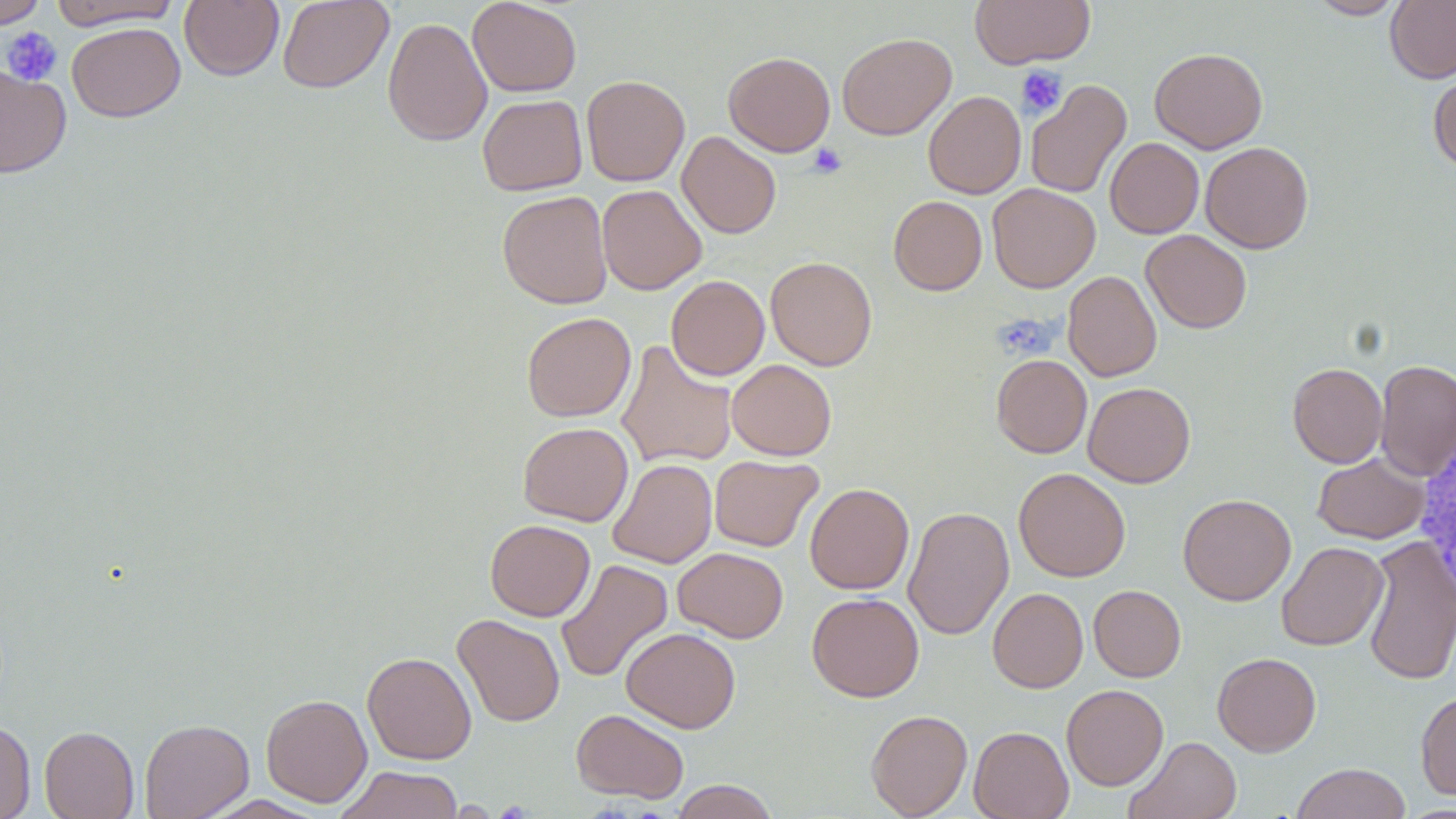

slide-level diagnosis = negative for blood parasites
magnification = 1000x
image size = 1456×819 pixels
uninfected red blood cell locations = approximate bounding boxes as [x1, y1, x2, y2] in pixels: [0, 0, 46, 29], [46, 0, 183, 30], [277, 0, 394, 93], [467, 0, 582, 97], [970, 0, 1095, 69], [1309, 0, 1406, 19], [1385, 0, 1456, 83], [179, 1, 284, 81], [382, 16, 493, 147], [66, 22, 185, 122], [837, 32, 956, 140], [1150, 47, 1267, 153], [723, 51, 835, 156], [0, 65, 71, 180], [1428, 68, 1456, 174], [581, 75, 690, 186], [1024, 79, 1132, 200], [923, 91, 1026, 199], [477, 94, 587, 195], [677, 131, 781, 239], [1105, 137, 1204, 238], [1200, 141, 1314, 253], [987, 183, 1101, 292], [596, 184, 706, 295], [497, 190, 612, 308], [888, 196, 987, 295], [1141, 230, 1252, 333], [765, 256, 878, 371], [1062, 270, 1162, 381], [666, 275, 769, 380], [521, 312, 636, 421], [616, 340, 738, 469], [991, 354, 1092, 458], [726, 359, 837, 460], [1375, 359, 1456, 480], [1288, 363, 1387, 468], [1082, 382, 1195, 487], [518, 422, 633, 526], [1313, 452, 1430, 544], [709, 455, 823, 551], [608, 458, 717, 568], [1013, 467, 1131, 581], [804, 483, 914, 594], [1177, 493, 1296, 606], [902, 506, 1014, 640], [485, 519, 596, 621], [1363, 536, 1456, 686], [1276, 542, 1388, 651], [673, 547, 788, 643], [556, 559, 673, 683], [1088, 585, 1186, 682], [987, 587, 1088, 693], [807, 592, 924, 702], [452, 614, 565, 727], [621, 627, 740, 733], [362, 651, 477, 765], [1212, 652, 1322, 756], [1061, 684, 1169, 791], [1416, 689, 1456, 800], [261, 693, 372, 807], [571, 708, 689, 804], [865, 709, 973, 818], [139, 718, 254, 819], [0, 720, 36, 819], [39, 726, 139, 819], [968, 726, 1073, 819], [1125, 736, 1242, 819], [1291, 762, 1412, 819], [335, 765, 465, 819], [670, 780, 779, 819]
white blood cell locations = approximate bounding boxes as [x1, y1, x2, y2] in pixels: [1413, 429, 1456, 607]
platelet locations = approximate bounding boxes as [x1, y1, x2, y2] in pixels: [1, 27, 63, 86], [1016, 65, 1067, 118], [807, 143, 847, 179], [992, 313, 1057, 360]
modality = light microscopy
field of view = single
preparation = thin blood smear
stain = May-Grünwald-Giemsa